Classify this cell by malaria status.
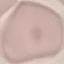

Uninfected.

Summary:
  - Image type: automatically extracted cell patch, resized to 64 × 64 pixels
  - Preparation: thin blood smear
  - Stain: Giemsa
  - Capture: smartphone camera at the microscope eyepiece